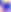
{
  "identification": "Toxoplasma gondii",
  "modality": "photomicrograph",
  "magnification": "400x"
}